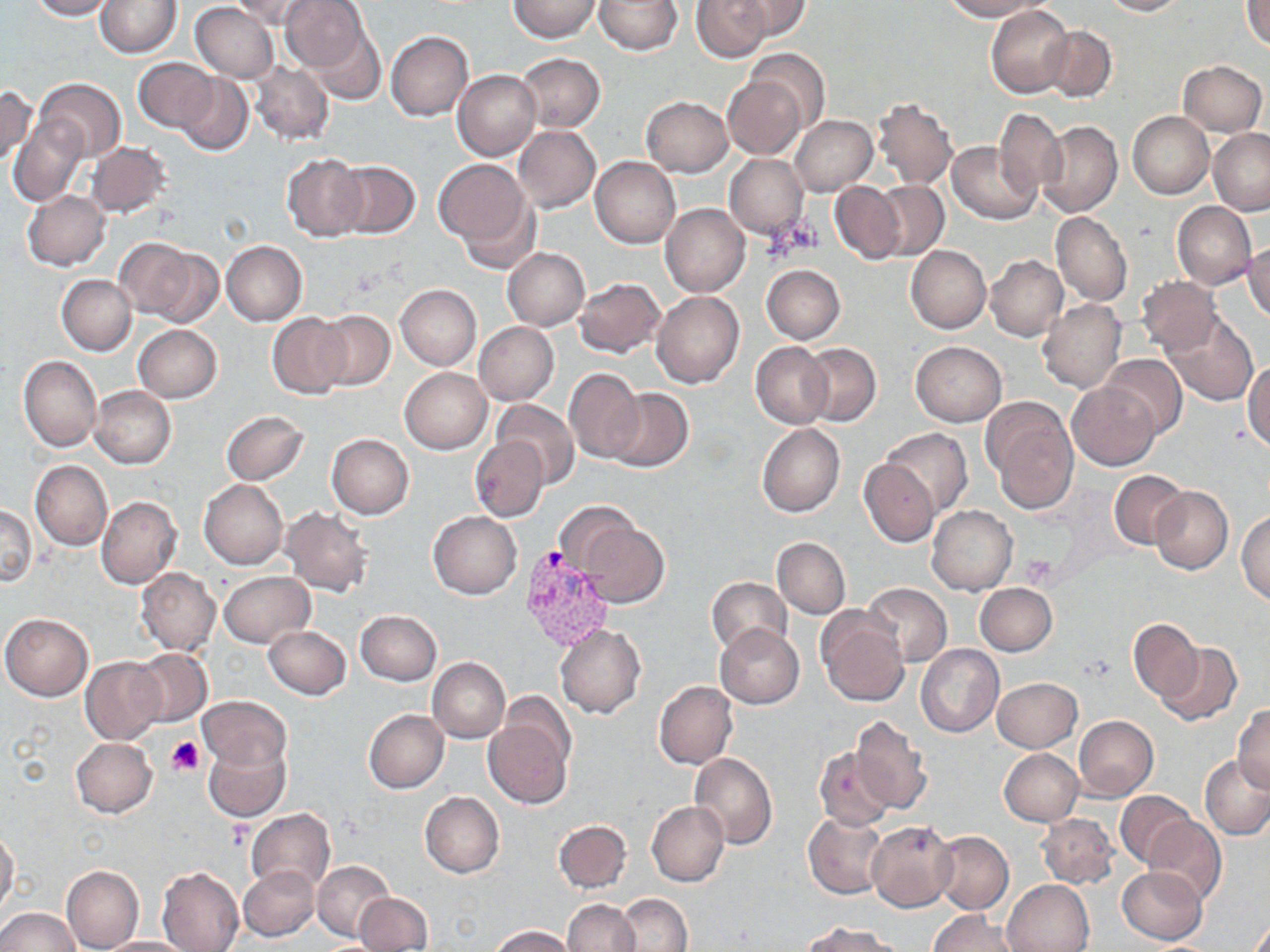
Summary:
  - Coordinate format: approximate bounding boxes as [x1, y1, x2, y2] in pixels
  - Uninfected red blood cell locations: [26, 0, 115, 21], [96, 0, 180, 57], [230, 0, 319, 30], [280, 0, 370, 73], [508, 0, 602, 41], [594, 0, 683, 54], [692, 0, 770, 62], [733, 0, 811, 40], [941, 0, 1044, 21], [1100, 0, 1189, 16], [1242, 0, 1270, 49], [190, 3, 280, 82], [986, 4, 1073, 98], [306, 23, 385, 105], [1041, 24, 1116, 102], [386, 31, 474, 121], [746, 48, 830, 133], [515, 52, 605, 132], [134, 58, 219, 133], [1178, 60, 1267, 135], [249, 62, 335, 145], [453, 70, 540, 161], [176, 74, 254, 155], [723, 75, 807, 159], [34, 78, 125, 161], [0, 87, 36, 167], [872, 96, 958, 189], [641, 97, 733, 177], [995, 108, 1065, 196], [1128, 111, 1213, 199], [10, 115, 87, 206], [790, 115, 877, 196], [1037, 120, 1122, 218], [513, 125, 600, 213], [1209, 128, 1270, 215], [86, 142, 171, 218], [948, 142, 1041, 224], [281, 153, 367, 241], [724, 154, 809, 241], [434, 157, 534, 251], [592, 157, 681, 248], [333, 161, 421, 239], [871, 181, 949, 260], [830, 182, 905, 264], [22, 190, 111, 271], [458, 197, 542, 275], [1171, 202, 1256, 288], [661, 203, 749, 297], [1051, 211, 1131, 307], [114, 238, 210, 324], [1246, 239, 1270, 323], [221, 240, 307, 325], [906, 245, 990, 334], [503, 247, 590, 330], [986, 254, 1068, 341], [761, 264, 845, 343], [56, 274, 137, 356], [1135, 276, 1222, 356], [574, 277, 666, 357], [395, 284, 481, 370], [652, 291, 744, 388], [1038, 298, 1127, 393], [313, 309, 396, 390], [267, 312, 350, 398], [1163, 314, 1257, 406], [474, 322, 558, 405], [134, 325, 222, 402], [910, 341, 1007, 427], [751, 342, 832, 430], [801, 342, 881, 426], [1102, 353, 1186, 437], [18, 355, 102, 452], [1245, 362, 1270, 451], [401, 367, 493, 453], [564, 368, 645, 463], [1068, 382, 1161, 470], [89, 385, 175, 469], [606, 387, 693, 472], [983, 398, 1079, 512], [492, 399, 580, 487], [221, 410, 309, 485], [757, 424, 845, 518], [880, 428, 972, 517], [327, 433, 414, 519], [469, 437, 549, 523], [859, 459, 937, 547], [30, 462, 112, 549], [1109, 471, 1187, 549], [199, 479, 288, 569], [1151, 487, 1233, 574], [97, 496, 181, 589], [553, 501, 645, 579], [0, 503, 38, 588], [927, 505, 1017, 596], [281, 507, 373, 597], [428, 511, 521, 599], [1237, 511, 1270, 604], [579, 521, 669, 609], [772, 537, 851, 619], [137, 567, 220, 654], [219, 571, 314, 647], [706, 577, 793, 655], [862, 582, 951, 667], [975, 582, 1056, 656], [356, 610, 442, 685], [817, 610, 909, 707], [1, 613, 93, 701], [1128, 619, 1204, 701], [555, 623, 646, 718], [715, 623, 804, 708], [264, 625, 351, 699], [1155, 643, 1242, 725], [916, 644, 1004, 737], [132, 649, 212, 726], [81, 656, 165, 744], [427, 658, 510, 743], [992, 677, 1082, 752], [654, 681, 737, 770], [198, 695, 290, 770], [1232, 704, 1270, 793], [484, 709, 575, 812], [364, 710, 449, 793], [849, 715, 932, 815], [1073, 716, 1158, 801], [71, 737, 158, 818], [203, 737, 290, 821], [814, 745, 895, 831], [999, 748, 1084, 826], [690, 752, 777, 849], [1201, 756, 1270, 840], [1115, 790, 1194, 869], [420, 792, 505, 878], [647, 801, 728, 886], [1037, 802, 1199, 876], [246, 808, 335, 894], [804, 813, 887, 899], [1037, 813, 1117, 889], [1144, 816, 1227, 905], [553, 819, 631, 892], [866, 820, 957, 912], [0, 826, 19, 918], [932, 830, 1014, 914], [313, 860, 393, 940], [238, 864, 321, 942], [60, 865, 144, 952], [156, 867, 244, 952], [1116, 867, 1207, 945], [1003, 879, 1094, 952], [355, 893, 432, 951], [617, 893, 691, 951], [562, 899, 640, 952], [0, 907, 80, 951], [929, 911, 1020, 952], [1246, 915, 1270, 952], [805, 921, 897, 952], [490, 925, 575, 952], [97, 936, 198, 952]
  - Platelet locations: [1020, 554, 1057, 587], [167, 737, 206, 777], [228, 822, 253, 848]
  - Plasmodium vivax-infected red blood cell locations: [517, 545, 615, 651]
  - Slide-level diagnosis: Plasmodium vivax
  - Preparation: thin blood film
  - Field of view: single
  - Stain: May-Grünwald-Giemsa
  - Modality: optical microscopy
  - Image size: 1270×952 pixels
  - Magnification: 1000x